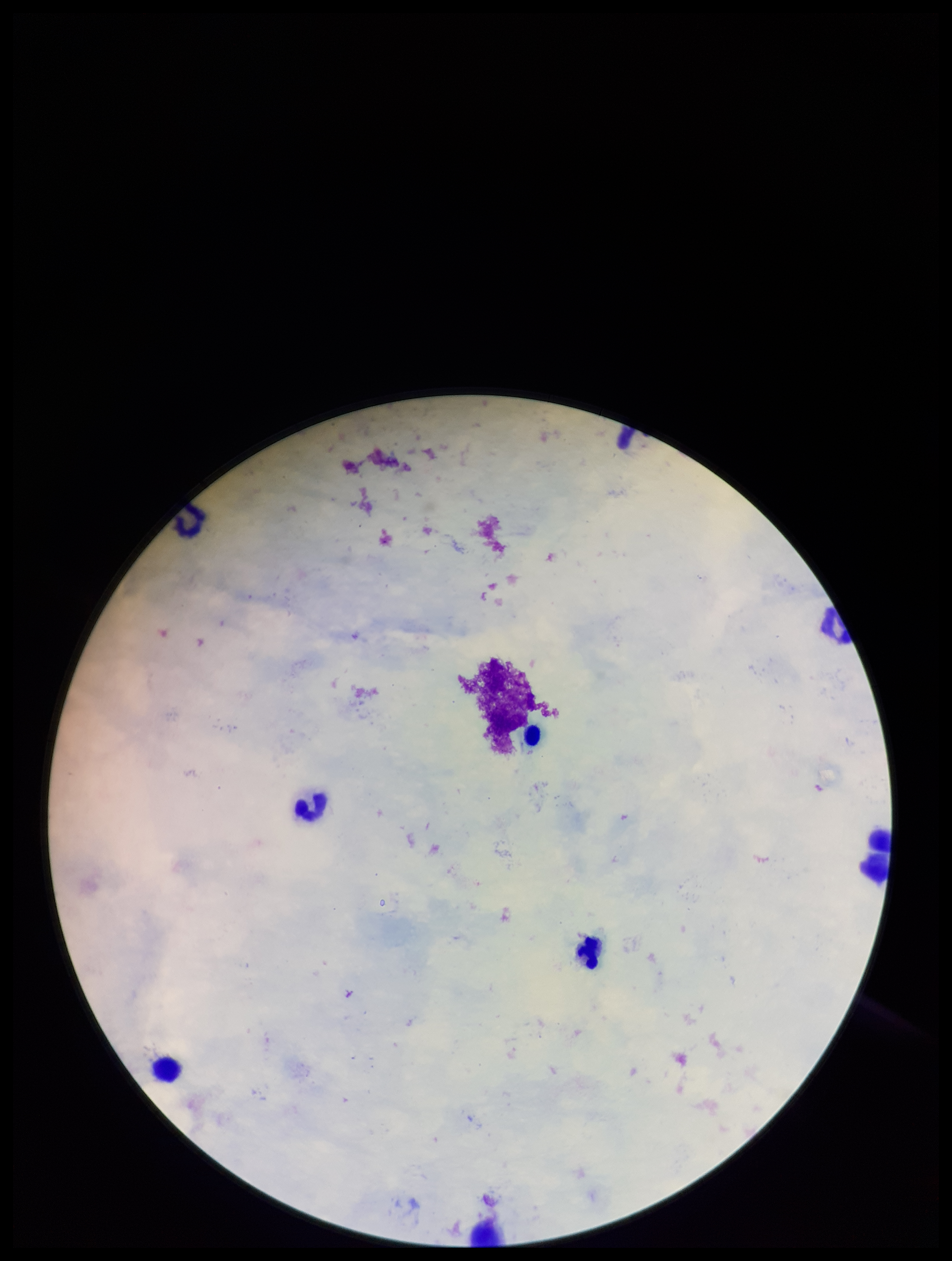 Smartphone photograph taken through the eyepiece of a microscope. Giemsa stain. One field from this slide. Leukocyte count: 6. Image is 952×1261 pixels. Plasmodium parasites: none seen. Preparation: thick blood smear. Parasite count: 0. Patient malaria status: negative.